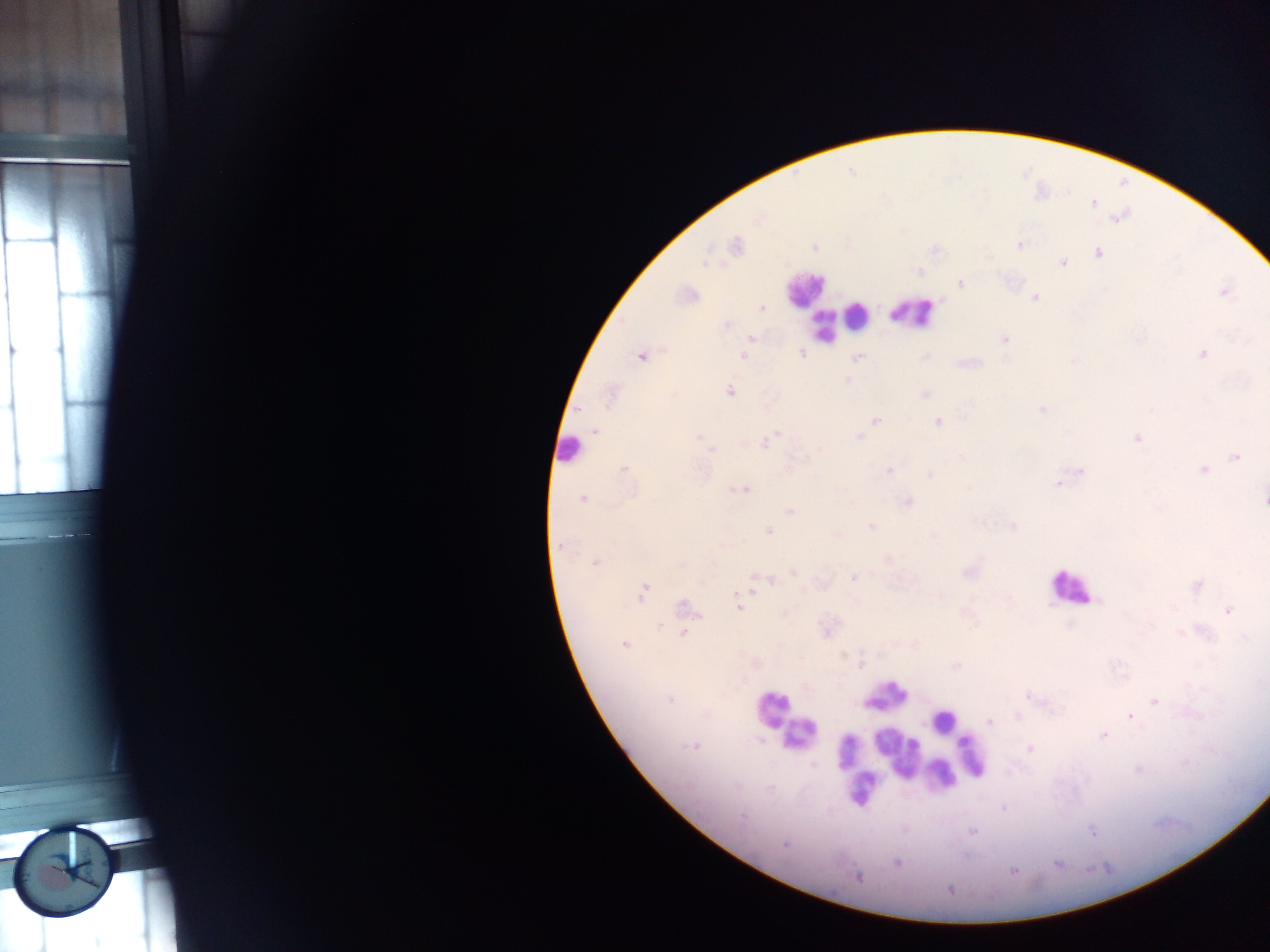
Approximate centers as x y in pixels. Object labeled both Plasmodium parasite and leukocyte by the source: 798 733. Leukocyte locations (subset; some below the resolvable size): 802 288; 914 313; 855 315; 823 328; 568 449; 1071 587; 773 707; 943 720; 897 752; 972 756; 862 787. Plasmodium parasite locations: 1093 204; 758 219; 1018 245; 735 246; 814 247; 1098 253; 705 261; 1063 262; 919 270; 960 283; 1225 293; 689 294; 1036 298; 762 307; 727 325; 751 337; 1005 339; 802 353; 1202 354; 743 356; 640 357; 858 357; 847 380; 729 391; 924 394; 610 397; 1043 410; 875 420; 939 421; 595 431; 773 436; 699 437; 858 437; 1137 438; 767 441; 712 450; 963 457; 1236 457; 623 469; 1203 469; 889 471; 1080 471; 930 474; 1058 483; 969 487; 741 490; 582 499; 1264 499; 908 501; 790 511; 872 526; 1012 526; 768 531; 837 534; 932 536; 558 547; 595 562; 794 573; 969 573; 853 577; 771 580; 1196 586; 643 590; 747 591; 684 605; 739 607; 1228 610; 660 625; 683 634; 1244 636; 623 644; 860 664; 955 666; 1028 696; 669 699; 1155 701; 1018 716; 1130 716; 990 722; 1102 736; 761 740; 692 746; 1030 749; 1186 762; 814 764; 1139 770; 737 786; 771 789; 1003 809; 742 816; 973 832; 1092 833; 785 845; 897 863; 1012 871; 857 877; 949 890. Photographed through a microscope with a mobile-phone camera. Image is 1270×952 pixels. Thick blood film. Collected in Ghana. One field of view.